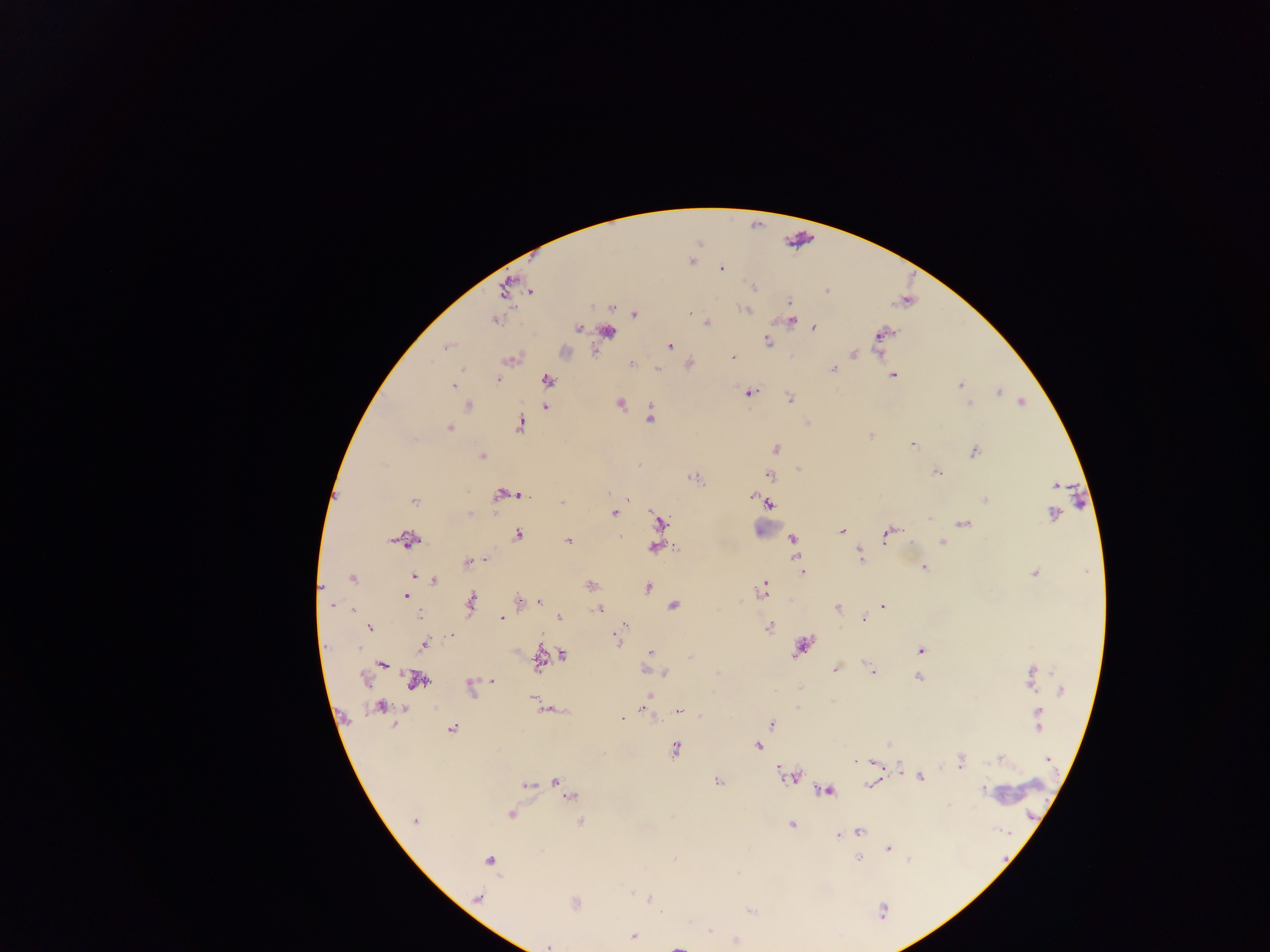 Approximate centers as [x, y] in pixels. Malaria parasite locations: [721, 268], [753, 289], [789, 302], [746, 311], [691, 312], [792, 319], [707, 322], [579, 328], [815, 328], [606, 331], [881, 333], [876, 338], [767, 341], [669, 345], [448, 349], [854, 353], [734, 357], [630, 361], [833, 368], [893, 375], [497, 379], [547, 380], [959, 385], [454, 386], [750, 392], [997, 392], [789, 398], [621, 403], [969, 403], [1022, 403], [470, 405], [544, 407], [650, 417], [520, 422], [450, 427], [869, 434], [912, 444], [775, 448], [974, 451], [482, 456], [936, 471], [769, 475], [1055, 484], [501, 492], [514, 494], [519, 494], [751, 495], [496, 497], [627, 497], [985, 499], [415, 501], [562, 503], [770, 504], [613, 513], [1052, 514], [930, 519], [659, 521], [964, 523], [842, 531], [518, 534], [885, 535], [409, 540], [793, 540], [567, 541], [941, 541], [654, 547], [858, 554], [485, 559], [468, 560], [922, 566], [926, 566], [803, 571], [1034, 573], [414, 577], [352, 579], [433, 582], [589, 584], [649, 587], [322, 589], [763, 589], [407, 596], [538, 600], [519, 602], [471, 604], [673, 605], [883, 605], [333, 607], [350, 608], [837, 608], [598, 609], [420, 616], [502, 617], [559, 617], [863, 619], [623, 624], [368, 628], [769, 628], [619, 630], [451, 635], [618, 641], [424, 645], [803, 646], [359, 650], [919, 650], [649, 652], [561, 655], [539, 662], [382, 664], [868, 666], [648, 669], [835, 669], [664, 671], [873, 671], [916, 676], [363, 679], [1029, 679], [417, 680], [494, 681], [468, 683], [1031, 687], [1060, 690], [534, 697], [382, 706], [680, 710], [1038, 710], [648, 711], [628, 716], [623, 719], [771, 724], [1037, 728], [452, 729], [887, 744], [758, 748], [676, 749], [853, 758], [1001, 759], [1046, 760], [853, 761], [875, 761], [962, 761], [900, 769], [788, 777], [922, 779], [555, 781], [719, 782], [871, 784], [526, 785], [983, 789], [828, 790], [569, 797], [512, 815], [416, 821], [580, 821], [790, 825], [861, 832], [836, 835], [844, 835], [889, 848], [675, 859], [858, 859], [909, 859], [488, 861], [630, 892], [479, 897], [650, 898], [660, 909], [883, 909], [708, 930], [633, 937], [735, 940], [548, 946], [678, 946]. Thick blood smear. One field of view. Image is 1270×952 pixels. Mobile-phone photograph taken through the microscope. Sample from Ghana.